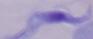
Summary:
  - Modality: micrograph
  - Identification: trypanosome
  - Magnification: 1000x